Locate every Trypanosoma brucei.
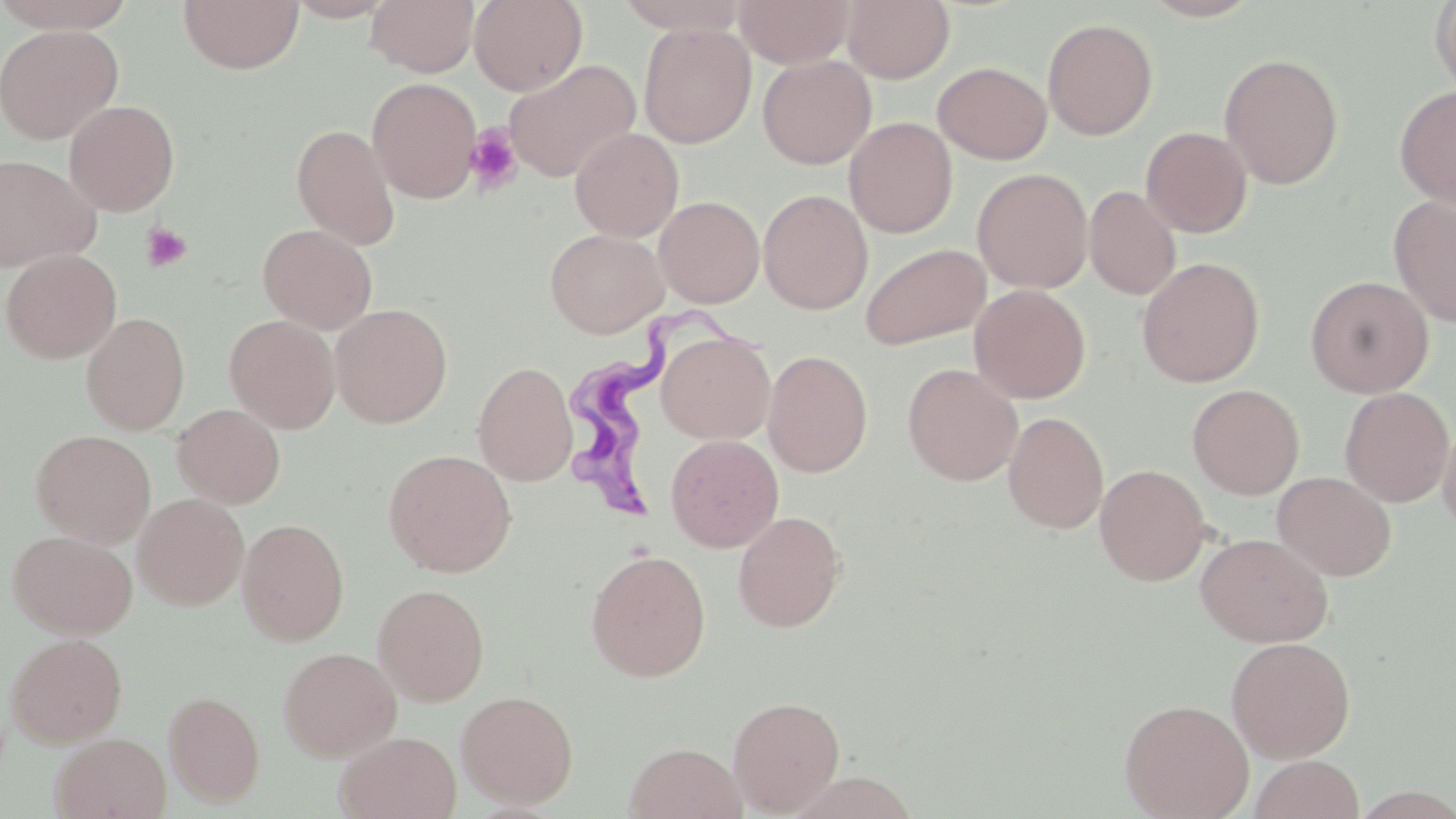

Approximate bounding boxes as (x1, y1, x2, y2) in pixels.
Trypanosoma brucei: (564, 308, 768, 525).

Summary:
  - Platelet locations: (464, 124, 523, 193), (140, 222, 193, 273)
  - Uninfected red blood cell locations: (0, 0, 139, 33), (178, 0, 304, 75), (366, 0, 479, 77), (469, 0, 587, 95), (614, 0, 752, 34), (735, 0, 855, 68), (842, 0, 954, 84), (1140, 0, 1265, 21), (1430, 0, 1456, 98), (1042, 18, 1159, 140), (638, 23, 756, 148), (0, 24, 123, 144), (1219, 52, 1344, 189), (757, 54, 876, 169), (504, 59, 641, 182), (933, 61, 1052, 164), (367, 77, 482, 203), (1395, 85, 1456, 209), (63, 99, 181, 216), (844, 117, 957, 238), (291, 124, 401, 250), (1140, 126, 1252, 238), (570, 127, 684, 242), (1, 153, 101, 271), (972, 167, 1093, 293), (1085, 185, 1181, 300), (758, 188, 873, 314), (1389, 195, 1456, 327), (654, 196, 764, 308), (258, 224, 377, 334), (545, 228, 668, 338), (860, 242, 991, 351), (1, 249, 122, 364), (1136, 257, 1264, 387), (1304, 275, 1434, 398), (969, 284, 1091, 403), (330, 303, 452, 428), (81, 312, 190, 434), (224, 314, 340, 433), (656, 329, 775, 445), (763, 349, 873, 477), (473, 360, 577, 486), (902, 362, 1022, 486), (1187, 383, 1305, 499), (1339, 387, 1454, 507), (172, 403, 285, 508), (1003, 411, 1108, 534), (1437, 417, 1456, 539), (30, 430, 156, 547), (665, 434, 784, 552), (383, 449, 517, 577), (1095, 464, 1212, 585), (1272, 471, 1397, 581), (133, 493, 249, 610), (732, 510, 846, 632), (237, 517, 349, 646), (7, 529, 137, 638), (1195, 532, 1333, 647), (585, 549, 711, 682), (372, 583, 490, 705), (5, 632, 128, 747), (1226, 636, 1356, 762), (278, 647, 401, 761), (164, 690, 266, 808), (456, 690, 578, 809), (728, 695, 846, 815), (1118, 698, 1255, 819), (335, 730, 462, 819), (50, 732, 172, 819), (624, 742, 747, 819), (1248, 755, 1364, 819)
  - Slide-level diagnosis: Trypanosoma brucei
  - Field of view: single
  - Magnification: 1000x
  - Image size: 1456×819 pixels
  - Modality: optical microscopy
  - Preparation: thin blood film
  - Stain: May-Grünwald-Giemsa